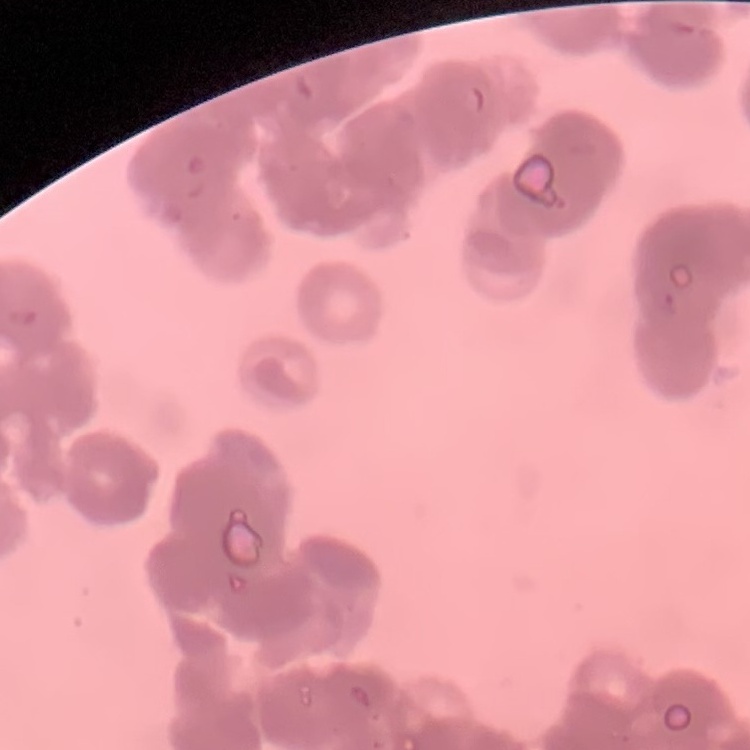

Summary:
  - Erythrocyte morphology: rouleaux formation
  - Stain: Field's or Giemsa
  - Preparation: thin blood film
  - Image type: square crop of a larger photomicrograph